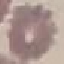
Result: no malaria parasites detected. Thin smear of blood. Giemsa stain. Photographed with a smartphone camera at the microscope eyepiece. Automatically extracted cell patch, resized to 64 × 64 pixels.